State which parasite is depicted.
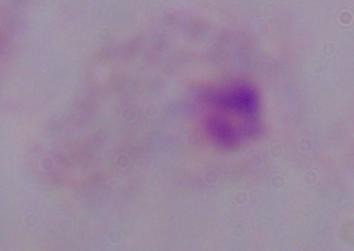
This is a trichomonad.

Summary:
  - Modality: micrograph
  - Magnification: 1000x